Report the malaria status of this cell.
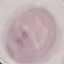

Uninfected.

preparation = thin blood film
stain = Giemsa
image type = cell patch, automatically extracted from a larger field of view and resized to 64 × 64 pixels
capture = smartphone camera at the microscope eyepiece